Assess this cell for malaria.
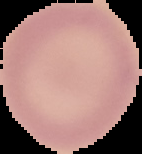

Uninfected.

Image is 142×154 pixels. The area outside the segmented cell region is set to black. From a thin blood film.